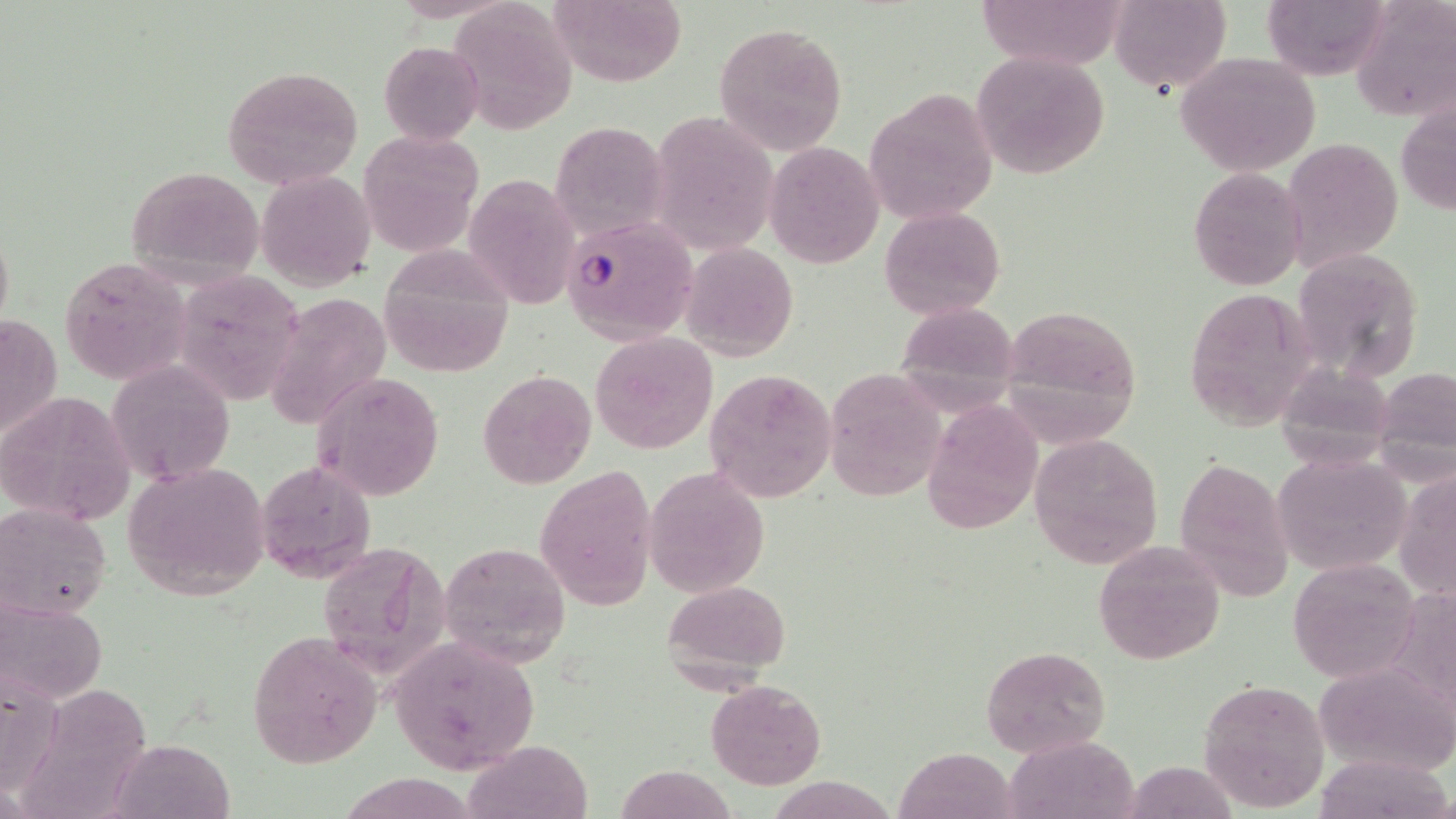 Approximate bounding boxes as (x1, y1, x2, y2) in pixels. Uninfected red blood cell locations: (443, 0, 579, 130), (544, 0, 688, 86), (975, 0, 1125, 73), (1110, 0, 1232, 95), (1263, 0, 1391, 80), (1353, 0, 1456, 124), (715, 22, 848, 157), (377, 40, 484, 144), (970, 51, 1109, 179), (1175, 52, 1321, 176), (221, 64, 365, 192), (865, 89, 998, 224), (1396, 97, 1456, 217), (660, 111, 778, 248), (549, 122, 667, 237), (359, 130, 484, 258), (1279, 137, 1403, 268), (764, 143, 883, 266), (123, 163, 266, 288), (1188, 166, 1308, 293), (257, 171, 375, 291), (472, 179, 579, 312), (880, 207, 1005, 320), (683, 242, 800, 361), (1296, 247, 1427, 379), (380, 252, 516, 377), (57, 255, 192, 385), (184, 267, 312, 409), (1183, 286, 1317, 433), (265, 289, 394, 430), (895, 298, 1020, 396), (999, 304, 1145, 440), (0, 310, 62, 449), (590, 332, 719, 454), (107, 360, 234, 483), (1375, 363, 1456, 472), (705, 368, 837, 502), (479, 369, 596, 490), (823, 369, 947, 500), (315, 372, 443, 501), (0, 389, 135, 526), (920, 397, 1045, 535), (1030, 432, 1163, 569), (1270, 453, 1412, 577), (1172, 456, 1295, 601), (256, 459, 378, 582), (124, 460, 270, 600), (535, 464, 655, 611), (645, 465, 769, 597), (1395, 467, 1456, 603), (2, 503, 112, 622), (313, 538, 451, 676), (1090, 541, 1225, 665), (437, 542, 570, 664), (1288, 558, 1421, 680), (661, 580, 792, 685), (0, 596, 107, 707), (248, 632, 382, 769), (386, 636, 541, 776), (980, 646, 1111, 757), (1315, 662, 1456, 778), (0, 674, 63, 795), (1196, 679, 1329, 811), (27, 680, 172, 819), (705, 681, 826, 790), (1005, 736, 1141, 818), (112, 738, 232, 818), (464, 739, 592, 819), (897, 748, 1018, 819), (1313, 751, 1454, 819), (611, 765, 740, 819). Plasmodium falciparum-infected red blood cell locations: (561, 214, 695, 343). Slide-level diagnosis: Plasmodium falciparum. May-Grünwald-Giemsa stain. Optical microscopy. Image is 1456×819 pixels. Captured at 1000x magnification. Thin blood smear. Single field of view.